Give the preparation type.
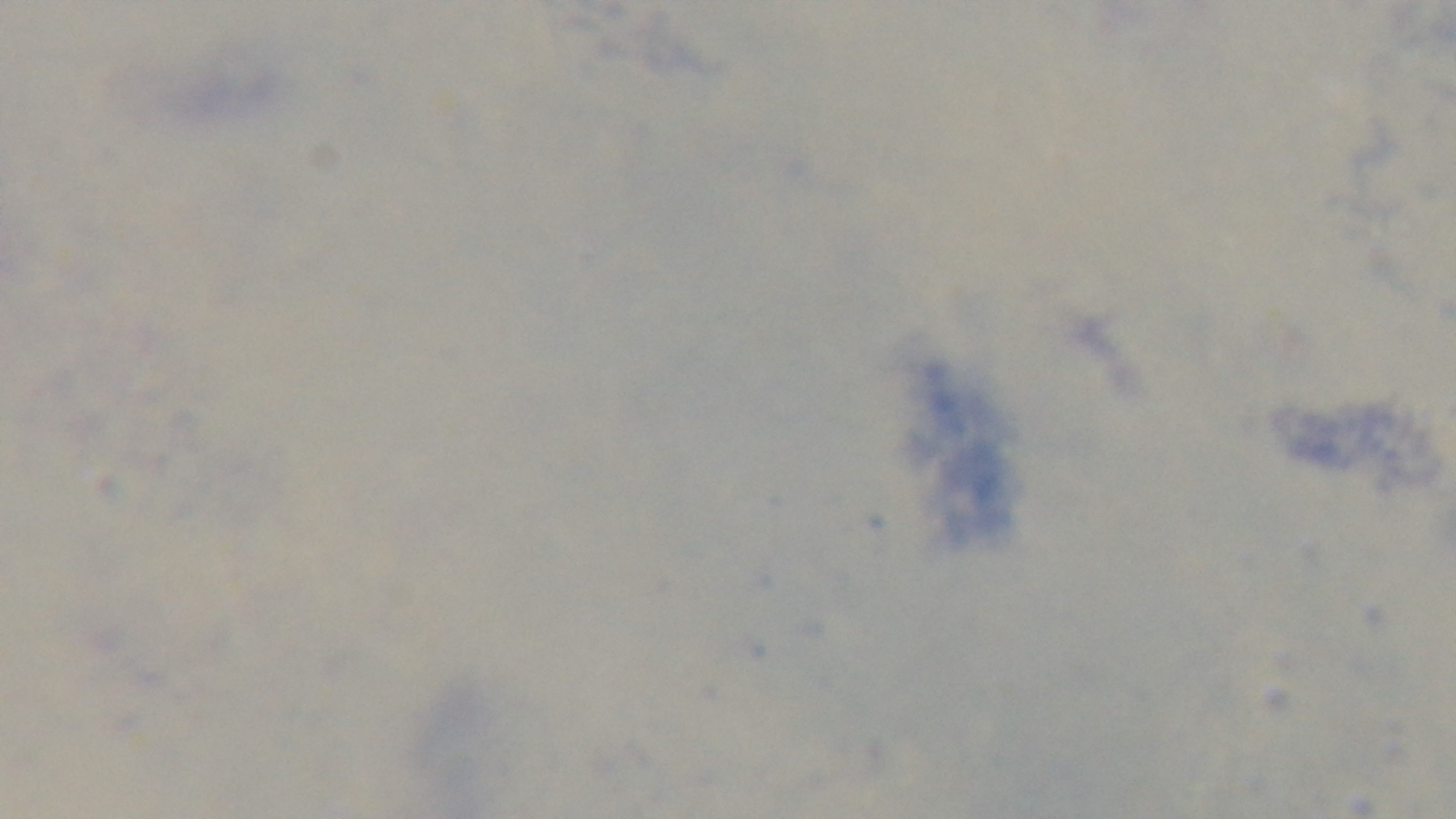
A thick smear.

Summary:
  - Stain: Giemsa
  - Malaria status: uninfected
  - Capture: mounted 4K digital camera
  - Field of view: single
  - Modality: light microscopy
  - Objective: 100x oil immersion